Locate every Plasmodium parasite.
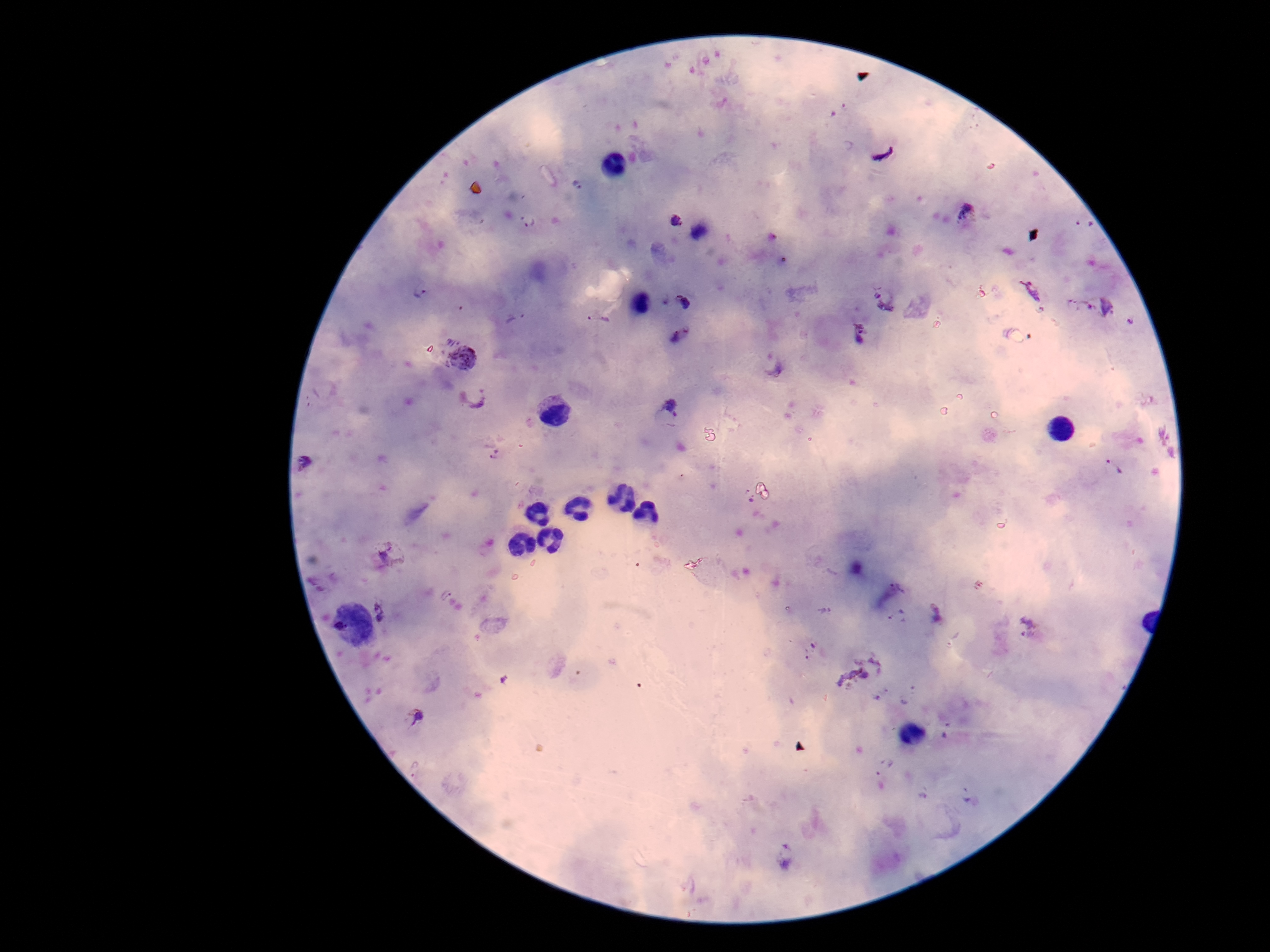

Approximate object centers, in pixels from the top-left corner.
Plasmodium parasites: (x=882, y=151), (x=578, y=185), (x=969, y=216), (x=529, y=220), (x=676, y=220), (x=1084, y=224), (x=422, y=291), (x=1033, y=291), (x=662, y=299), (x=884, y=300), (x=686, y=303), (x=1106, y=305), (x=1075, y=307), (x=515, y=318), (x=598, y=320), (x=1131, y=324), (x=860, y=333), (x=681, y=336), (x=464, y=358), (x=775, y=367), (x=473, y=399), (x=668, y=413), (x=495, y=456), (x=306, y=464), (x=1116, y=467), (x=748, y=495), (x=393, y=554), (x=897, y=590), (x=381, y=613), (x=936, y=614), (x=899, y=618), (x=1028, y=626), (x=811, y=652), (x=418, y=716), (x=884, y=767), (x=416, y=771), (x=968, y=793), (x=787, y=855).

preparation = thick peripheral-blood smear
field of view = single
image size = 1270×952 pixels
capture = smartphone camera through the microscope eyepiece
patient malaria status = positive
stain = Giemsa
magnification = 100x